Name the cell type shown.
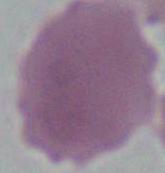
An erythrocyte.

Photomicrograph. 1000x magnification.